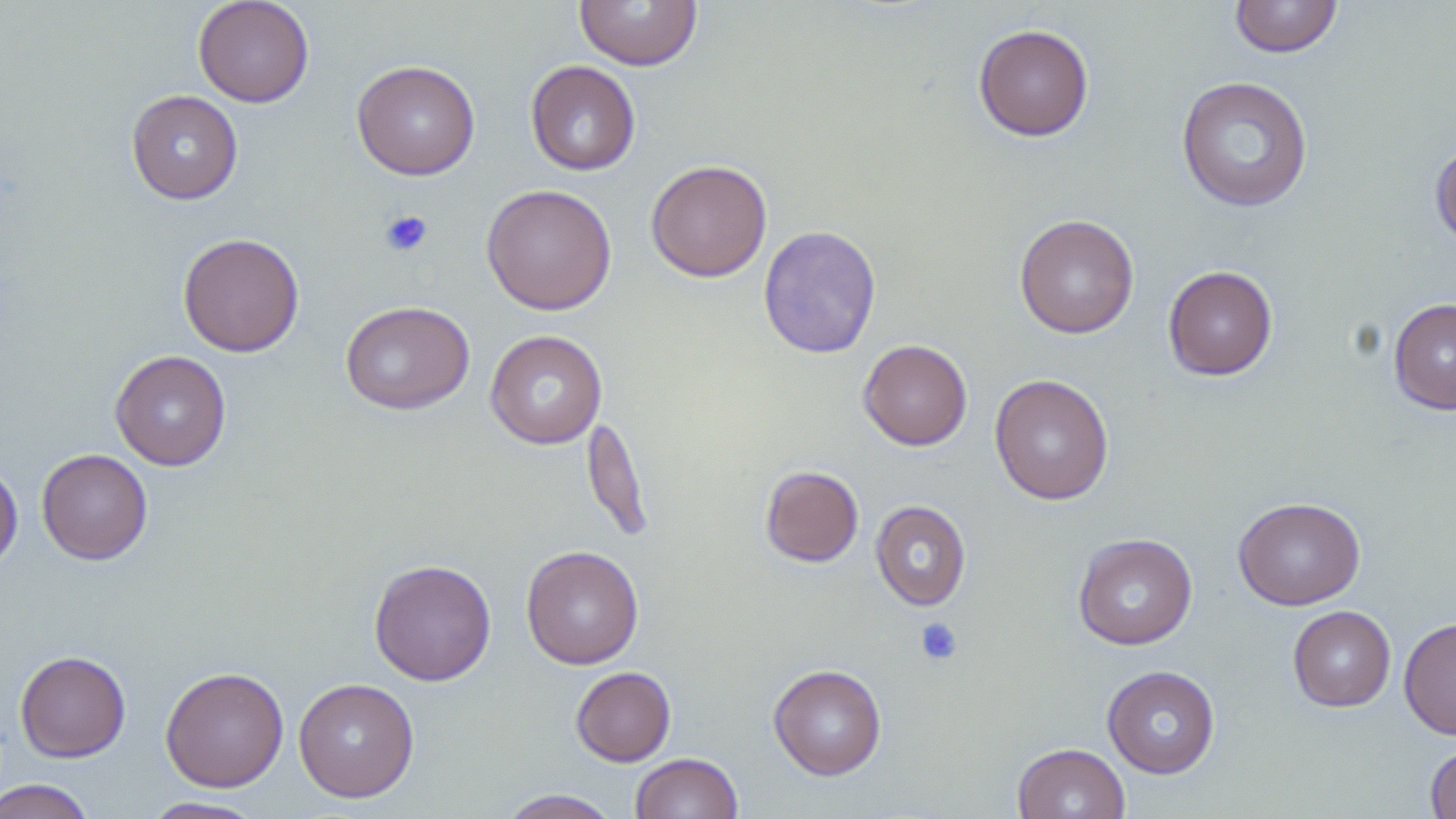

slide-level diagnosis = negative for blood parasites
uninfected red blood cell locations = approximate bounding boxes as (x1,y1)-(x2,y2) corner pairs in pixels: (193,0)-(314,107), (574,0)-(703,71), (1230,0)-(1342,58), (973,23)-(1094,141), (351,59)-(480,181), (525,60)-(641,176), (1176,76)-(1313,212), (126,90)-(243,204), (1430,139)-(1456,249), (646,159)-(772,282), (481,183)-(617,315), (1014,213)-(1140,338), (758,225)-(882,358), (178,232)-(305,357), (1163,265)-(1278,380), (1388,297)-(1456,415), (340,300)-(475,415), (485,330)-(607,449), (858,339)-(972,451), (110,350)-(232,471), (989,374)-(1114,505), (582,414)-(654,544), (36,448)-(153,565), (0,461)-(22,573), (760,465)-(864,567), (1234,497)-(1365,610), (870,500)-(971,611), (1072,533)-(1197,650), (520,545)-(644,670), (368,558)-(497,686), (1288,606)-(1396,712), (1398,617)-(1456,740), (15,650)-(131,762), (768,664)-(887,780), (1102,665)-(1220,778), (160,666)-(289,793), (570,666)-(676,766), (293,677)-(419,802), (1424,742)-(1456,819), (1013,743)-(1129,819), (631,753)-(743,819), (0,779)-(96,819), (499,789)-(621,818), (141,796)-(267,818)
platelet locations = approximate bounding boxes as (x1,y1)-(x2,y2) corner pairs in pixels: (378,209)-(433,257), (915,617)-(963,666)
preparation = thin blood film
magnification = 1000x
modality = optical microscopy
image size = 1456×819 pixels
field of view = one of a larger specimen
stain = May-Grünwald-Giemsa